Locate Plasmodium parasites and leukocytes.
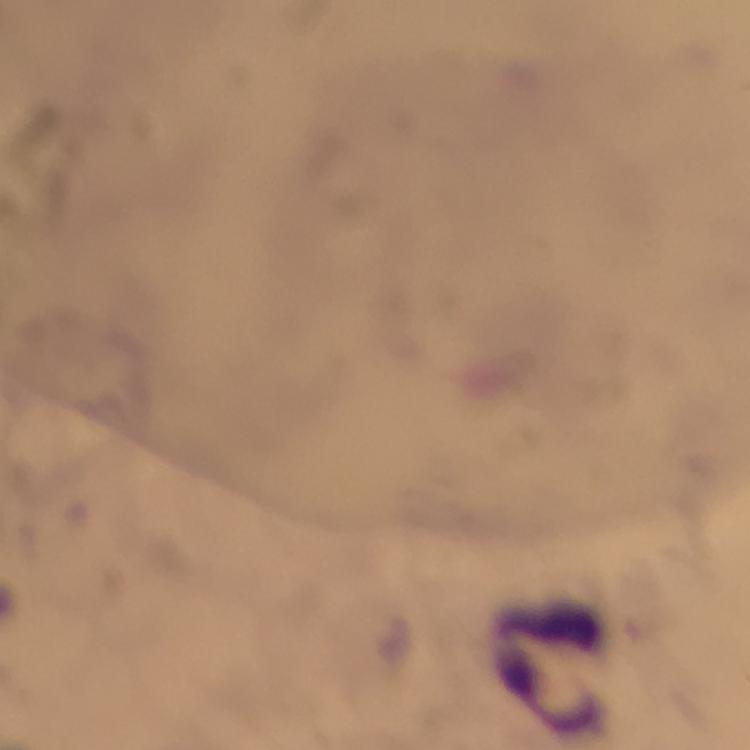
No Plasmodium parasites seen.
Approximate centers as [x, y] in pixels.
Leukocytes: [558, 669].

stain = Giemsa
immersion oil = used
capture = smartphone camera through the microscope
cropped from = a single field of view
magnification = 100x
context = from a malaria diagnostic workup
image size = 750×750 pixels
preparation = thick blood smear